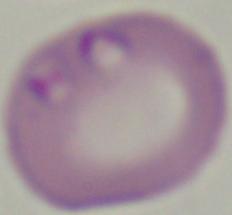 Photomicrograph. Captured at 1000x magnification. A Babesia parasite is shown.